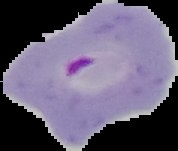 From a thin blood film. Result: malaria parasites identified. Image is 178×151 pixels. The area outside the segmented cell region is set to black.